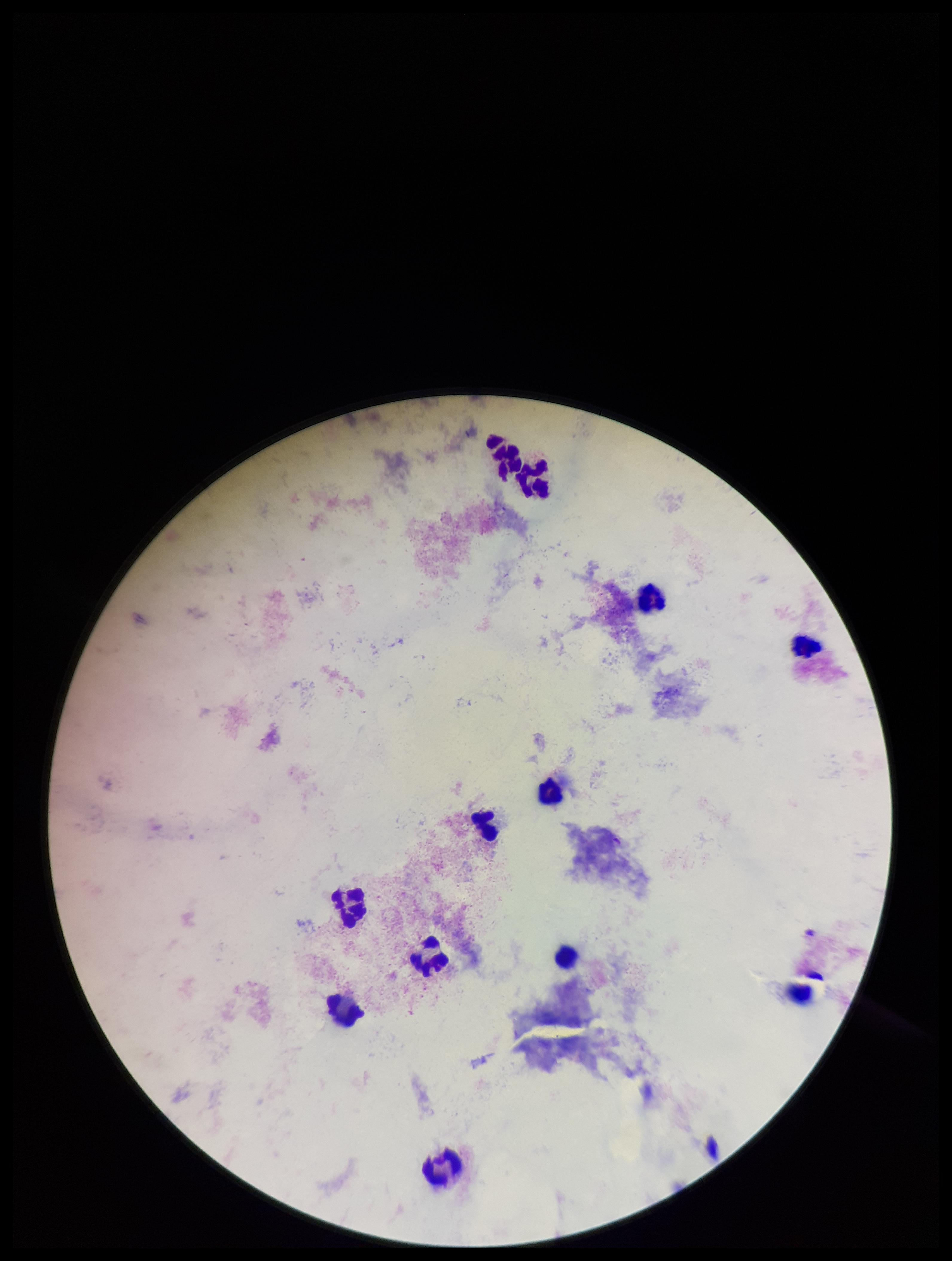
patient malaria status = negative
preparation = thick
stain = Giemsa
field of view = one from this slide
parasite count = 0
capture = smartphone photograph through the microscope eyepiece
leukocyte count = 11
image size = 952×1261 pixels
Plasmodium parasites = none detected